Assess this cell for malaria.
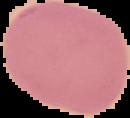
It is uninfected.

Summary:
  - Image size: 130×118 pixels
  - Image type: cell region segmented out of the field of view; surrounding area masked to black
  - Preparation: thin blood film